Report the malaria status of this cell.
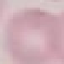

Uninfected.

{
  "preparation": "thin blood smear",
  "capture": "smartphone through the microscope eyepiece",
  "image_type": "cell patch, automatically extracted from a larger field of view and resized to 64 × 64 pixels",
  "stain": "Giemsa"
}